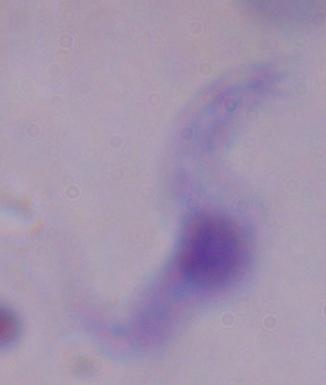
{
  "modality": "photomicrograph",
  "identification": "trypanosome",
  "magnification": "1000x"
}